Describe the morphology of the erythrocytes.
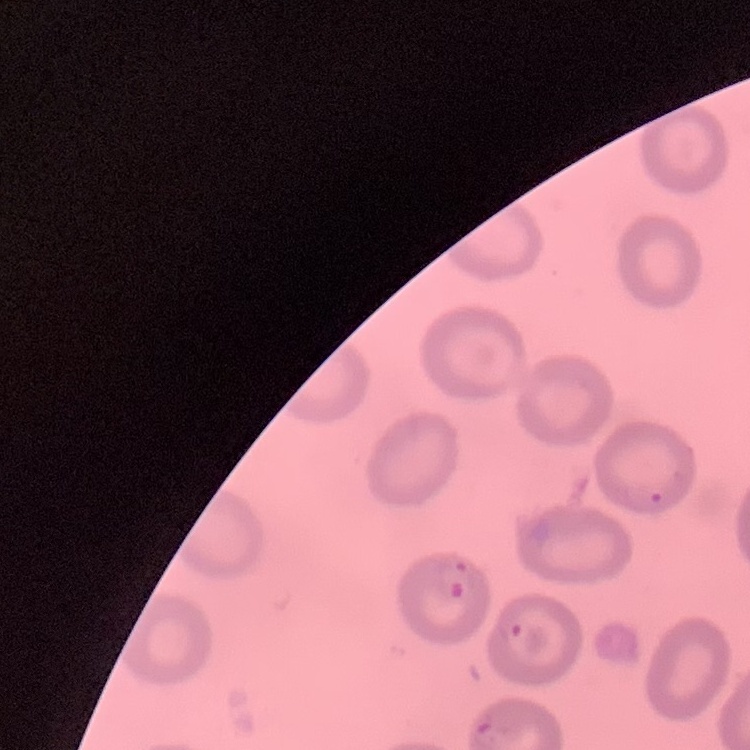

No rouleaux formation.

stain: Field's or Giemsa
image_type: square crop of a larger photomicrograph
preparation: thin blood smear